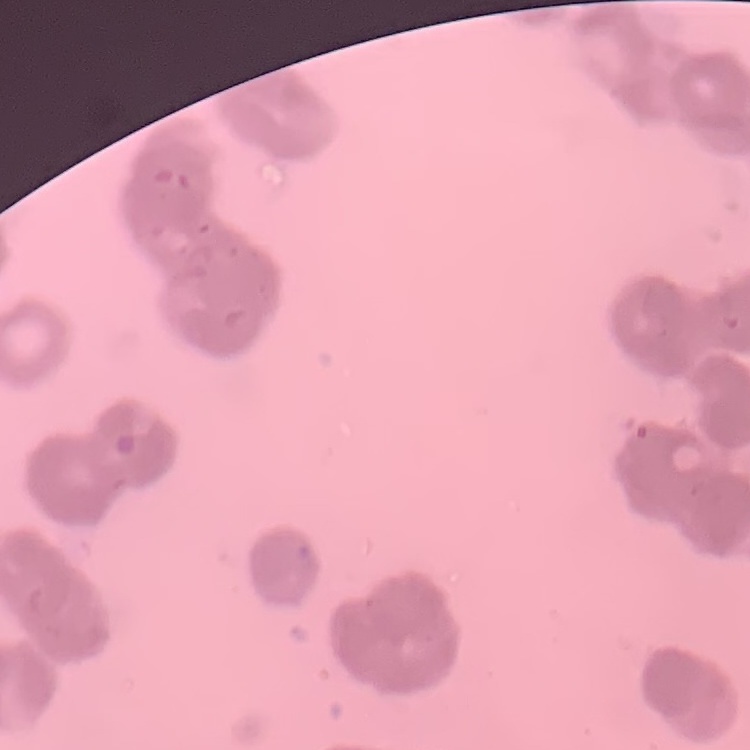

Summary:
  - Red blood cell morphology: rouleaux formation
  - Image type: one tile cut from a larger photomicrograph
  - Preparation: thin blood film
  - Stain: Field's or Giemsa